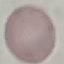

Summary:
  - Malaria status: uninfected
  - Stain: Giemsa
  - Capture: smartphone through the microscope eyepiece
  - Image type: automatically extracted cell patch, resized to 64 × 64 pixels
  - Preparation: thin smear